Classify this cell by malaria status.
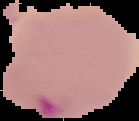

It is parasitized.

preparation = thin blood film
image type = cell region segmented out of the field of view; surrounding area masked to black
image size = 139×121 pixels